Identify the blood parasite species.
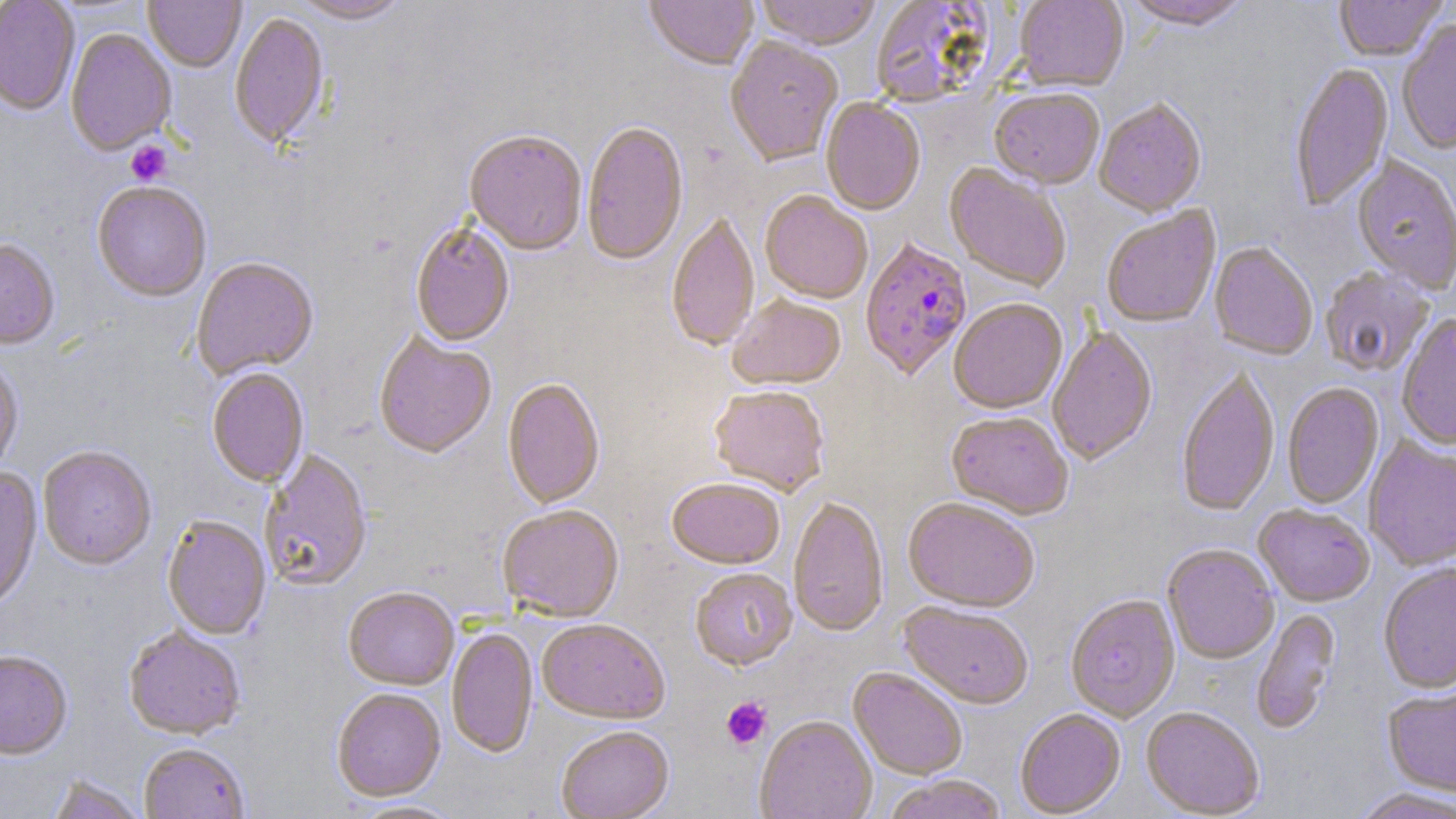

Plasmodium falciparum.

Approximate bounding boxes as [x1, y1, x2, y2] in pixels. Plasmodium falciparum-infected red blood cell locations: [860, 239, 973, 383]. Platelet locations: [126, 142, 172, 186], [721, 697, 772, 749]. Uninfected red blood cell locations: [144, 0, 245, 73], [290, 0, 412, 26], [644, 0, 758, 74], [754, 0, 881, 53], [1013, 0, 1128, 93], [1119, 0, 1252, 33], [1334, 0, 1447, 63], [0, 1, 80, 116], [869, 1, 996, 108], [229, 14, 329, 151], [1397, 23, 1456, 155], [65, 29, 176, 157], [725, 38, 843, 169], [1290, 65, 1394, 213], [989, 91, 1104, 191], [820, 99, 925, 217], [1094, 101, 1207, 219], [581, 123, 689, 268], [464, 133, 586, 257], [1351, 156, 1456, 295], [943, 164, 1071, 293], [92, 183, 211, 303], [760, 193, 872, 306], [1101, 207, 1221, 329], [667, 214, 759, 353], [410, 223, 515, 348], [0, 240, 60, 352], [1209, 243, 1317, 361], [192, 259, 318, 380], [1319, 267, 1434, 378], [728, 298, 846, 392], [949, 301, 1068, 416], [1397, 316, 1456, 451], [1047, 327, 1157, 466], [374, 333, 496, 460], [0, 360, 24, 477], [206, 368, 309, 488], [1176, 369, 1280, 519], [502, 378, 605, 510], [1282, 383, 1384, 510], [709, 388, 829, 498], [946, 413, 1073, 521], [1364, 438, 1456, 572], [38, 447, 156, 572], [259, 450, 373, 593], [0, 469, 42, 614], [666, 480, 785, 570], [788, 498, 889, 638], [902, 500, 1039, 614], [1253, 505, 1374, 608], [497, 507, 624, 622], [162, 518, 271, 640], [1163, 545, 1279, 666], [1379, 564, 1456, 695], [690, 569, 798, 672], [343, 588, 459, 692], [1065, 596, 1181, 723], [899, 603, 1033, 711], [1251, 608, 1341, 735], [537, 620, 669, 725], [123, 629, 245, 742], [447, 629, 538, 758], [0, 652, 72, 762], [848, 668, 968, 780], [1382, 689, 1456, 799], [332, 690, 446, 802], [1141, 708, 1264, 818], [1015, 710, 1126, 817], [755, 717, 877, 819], [555, 727, 674, 819], [139, 745, 251, 819], [47, 775, 145, 819], [881, 776, 1008, 819], [1351, 788, 1456, 819], [350, 800, 466, 819]. Thin blood film. Optical microscopy. Captured at 1000x magnification. Image is 1456×819 pixels. Single field of view. May-Grünwald-Giemsa-stained preparation.